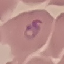

malaria status = parasitized
image type = automatically extracted cell patch, resized to 64 × 64 pixels
preparation = thin smear
capture = smartphone camera at the microscope eyepiece
stain = Giemsa